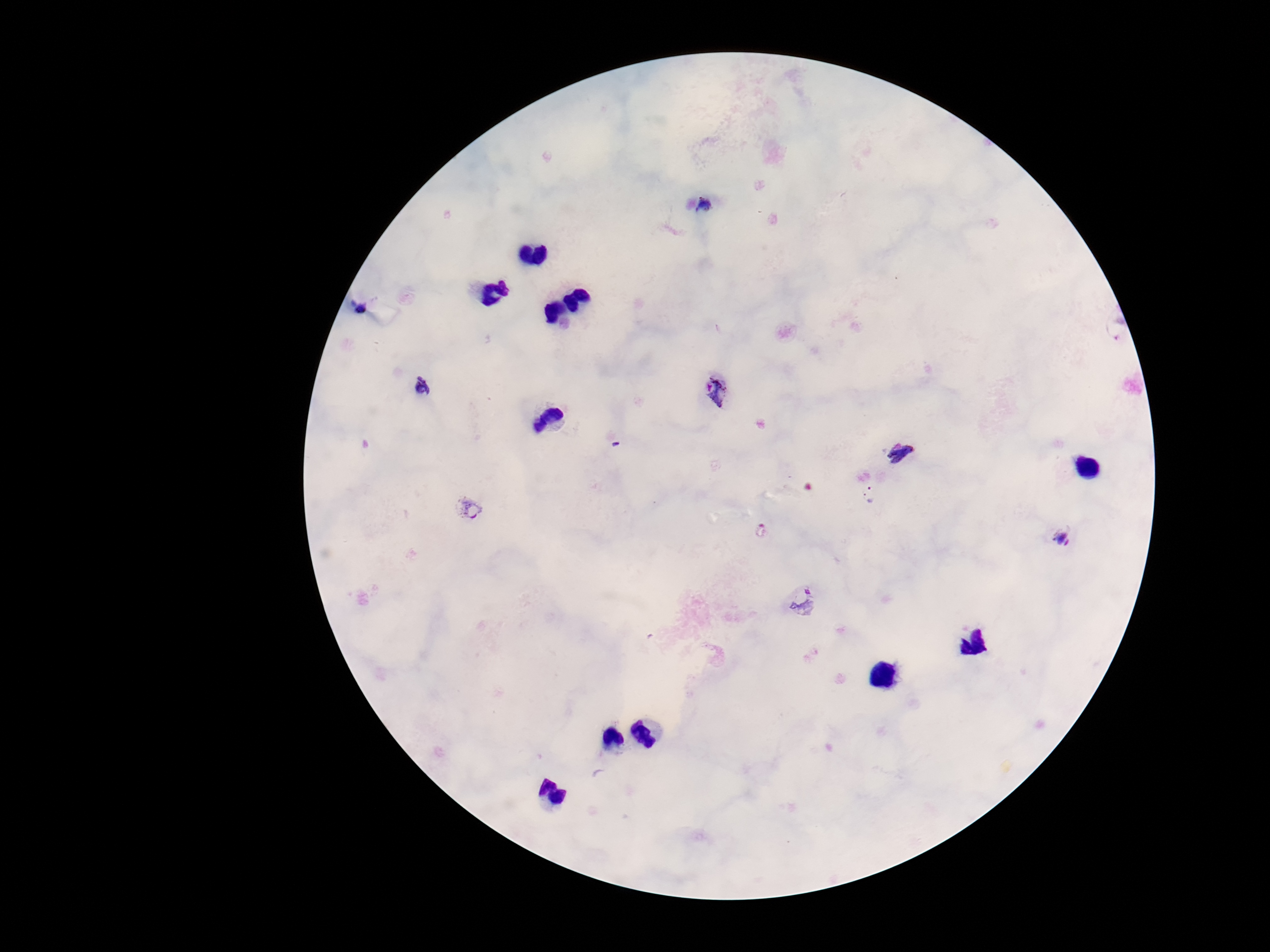

Approximate object centers, in pixels from the top-left corner.
Summary:
  - Plasmodium parasite locations: (x=704, y=205), (x=362, y=309), (x=421, y=390), (x=715, y=392), (x=901, y=453), (x=869, y=496), (x=469, y=507), (x=1061, y=537), (x=806, y=600)
  - Capture: smartphone camera through the microscope eyepiece
  - Preparation: thick peripheral-blood smear
  - Field of view: single
  - Patient malaria status: infected
  - Magnification: 100x
  - Image size: 1270×952 pixels
  - Stain: Giemsa